Rate the background quality.
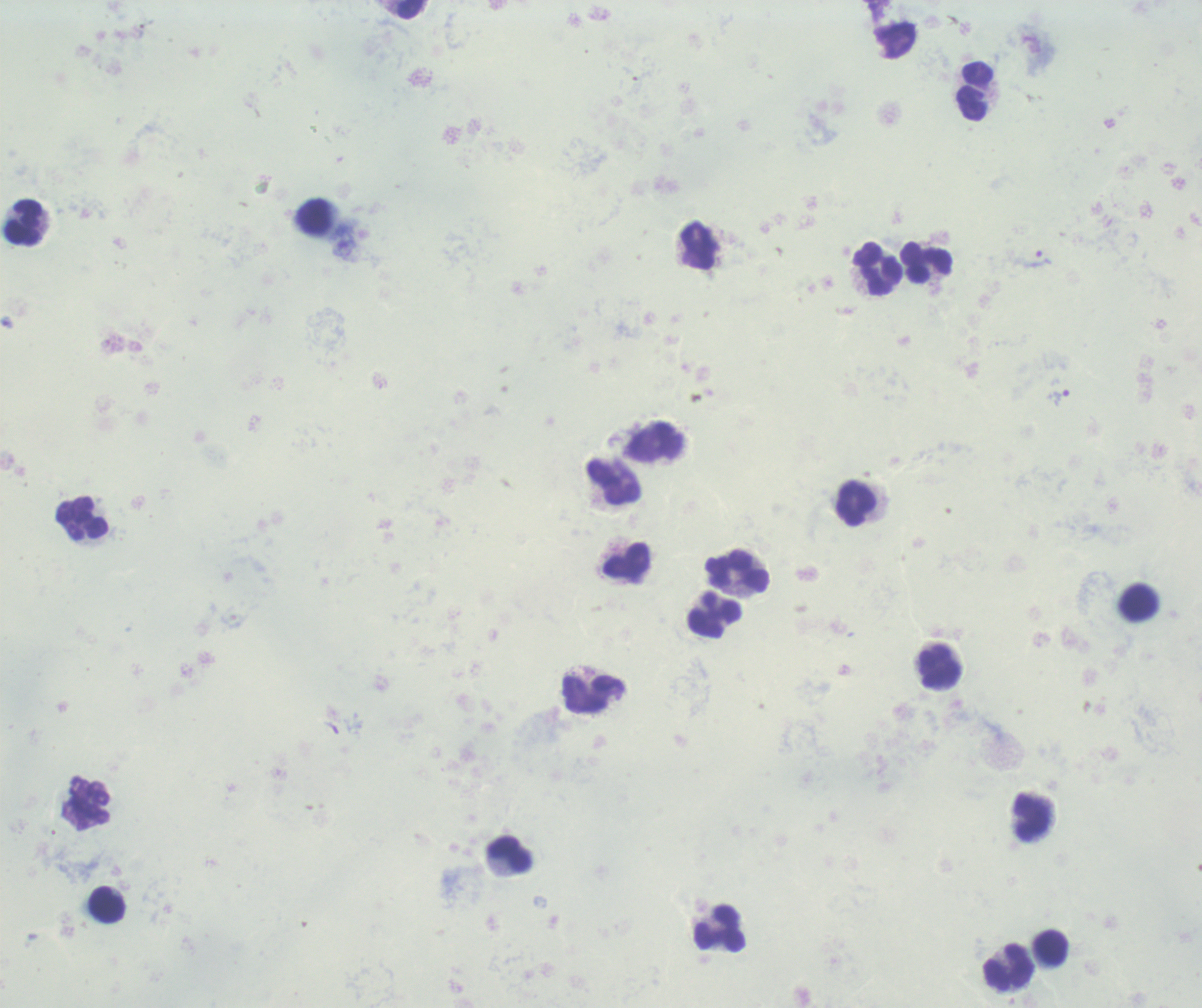
Poor.

coordinate format = approximate centers as [x, y] in pixels
trophozoite locations = [1040, 259], [1058, 396]
leukocyte locations = [410, 9], [975, 91], [314, 218], [24, 222], [926, 262], [876, 267], [613, 481], [855, 503], [82, 518], [627, 561], [738, 572], [1139, 602], [714, 620], [938, 668], [592, 694], [1031, 816], [509, 854], [108, 904], [720, 928], [1050, 947], [1008, 966]
stain = Romanowsky
context = previously used in a real diagnosis
result = malaria parasites identified
image size = 1202×1008 pixels
preparation = thick blood smear
magnification = 100x
field of view = single